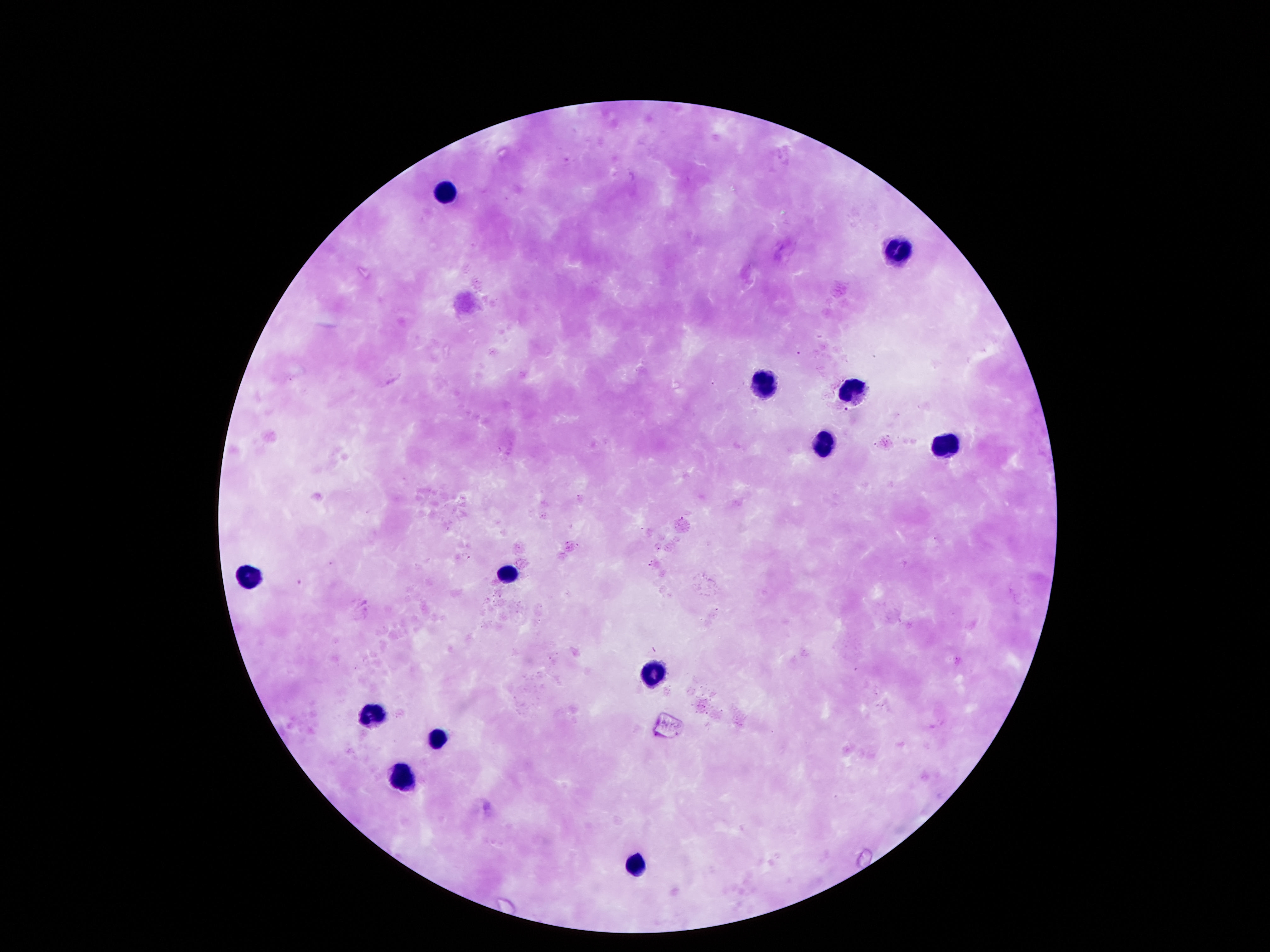

Approximate centers as [x, y] in pixels.
Summary:
  - Leukocyte locations: [444, 194], [901, 253], [766, 382], [854, 384], [945, 446], [820, 449], [511, 570], [249, 573], [652, 676], [370, 715], [434, 735], [403, 777], [635, 861]
  - Image size: 1270×952 pixels
  - Capture: smartphone camera through the microscope eyepiece
  - Magnification: 100x
  - Preparation: thick blood film
  - Stain: Giemsa
  - Field of view: one from this slide
  - Patient malaria status: not infected